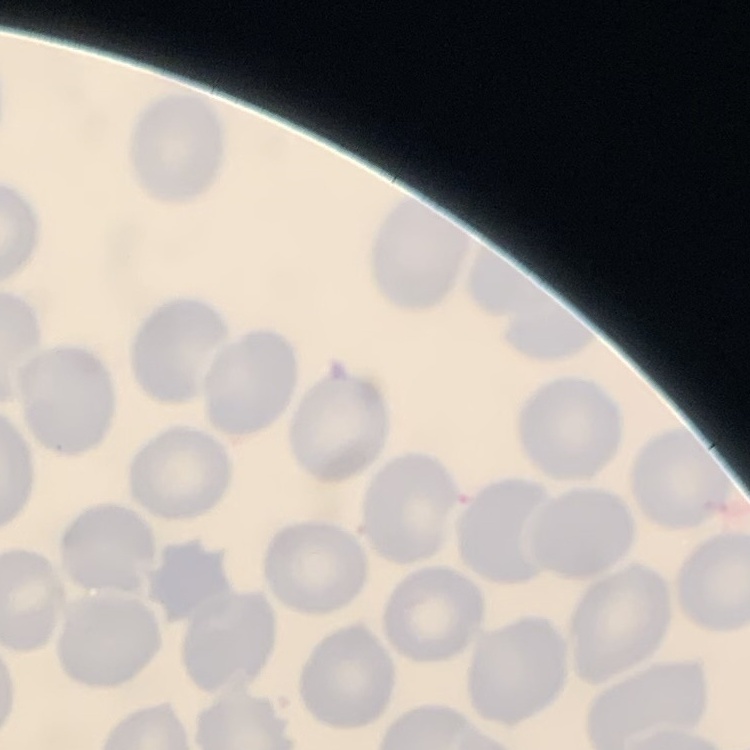
Summary:
  - Erythrocyte morphology: no rouleaux formation
  - Stain: Field's or Giemsa
  - Preparation: thin blood smear
  - Image type: one tile cut from a larger photomicrograph